Assess the morphology of the erythrocytes.
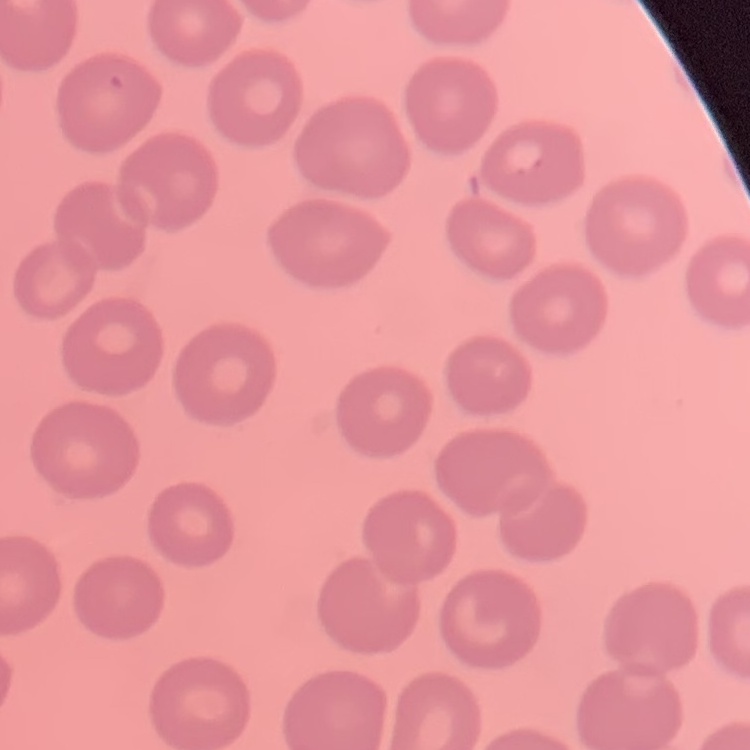
They show no rouleaux formation.

Summary:
  - Image type: one tile cut from a larger photomicrograph
  - Preparation: thin peripheral smear
  - Stain: Field's or Giemsa